Report the malaria status of this cell.
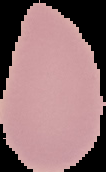
Uninfected.

Image is 106×172 pixels. The area outside the segmented cell region is set to black. From a thin blood film.